Classify this cell by malaria status.
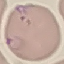

It is parasitized.

Summary:
  - Image type: cell patch, automatically extracted from a larger field of view and resized to 64 × 64 pixels
  - Capture: smartphone camera at the microscope eyepiece
  - Preparation: thin blood smear
  - Stain: Giemsa